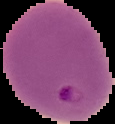 Image is 115×124 pixels. The area outside the segmented cell region is set to black. From a thin blood film. Result: Plasmodium parasites identified.